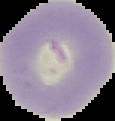
From a thin blood film. Image is 115×121 pixels. Result: no Plasmodium parasites seen. The area outside the segmented cell region is set to black.